Report the malaria status of this cell.
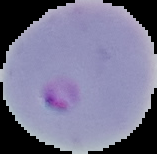

Parasitized.

Segmented cell region on a black background. Image is 157×154 pixels. From a thin blood smear.